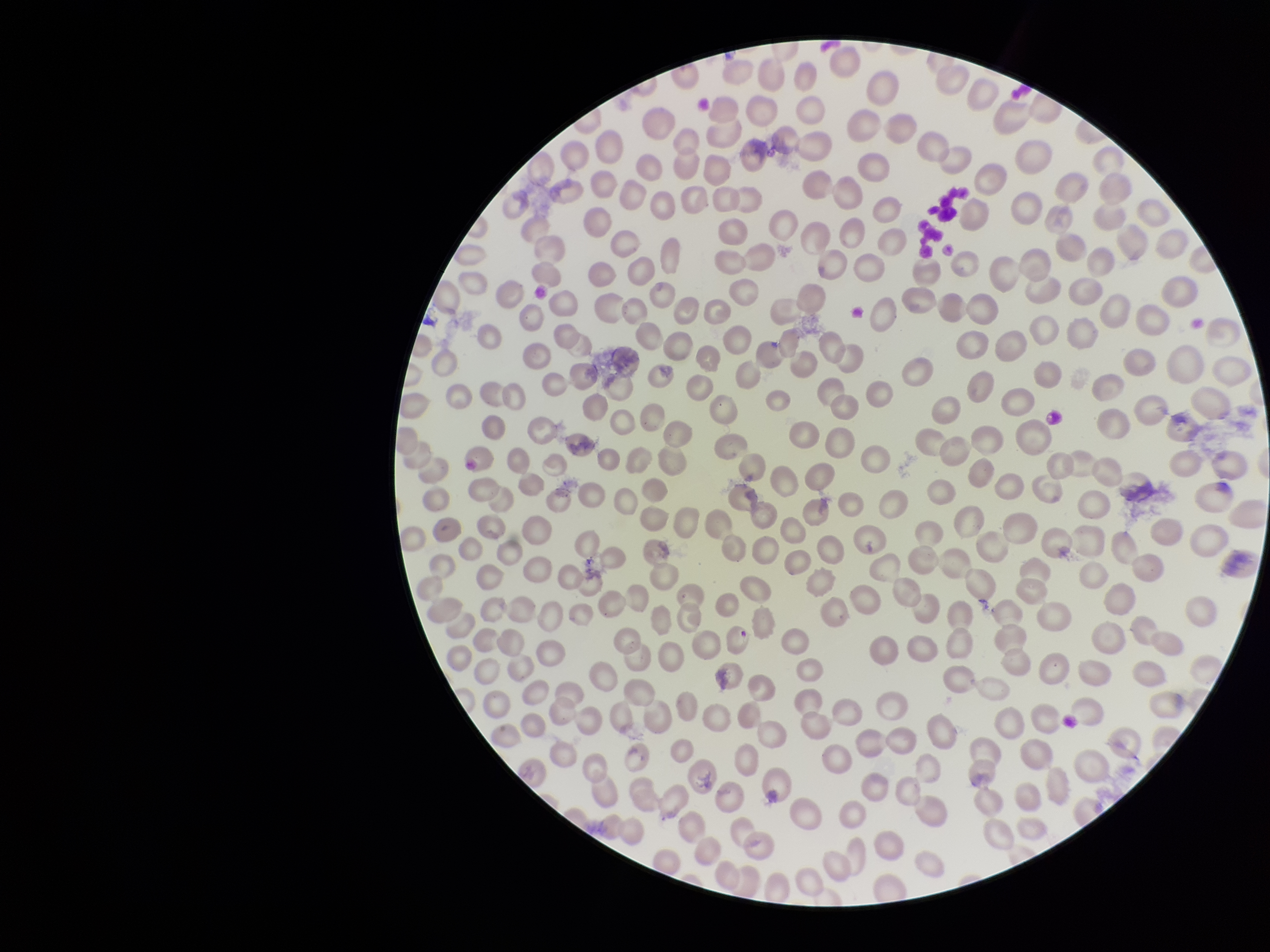

parasitized red blood cells = none detected
parasitized red blood cell count = 0
stain = Giemsa
image size = 1270×952 pixels
field of view = one from this slide
preparation = thin smear
red blood cell count = 303
capture = smartphone photograph through the microscope eyepiece
patient malaria status = infected
species reported for this patient = Plasmodium falciparum